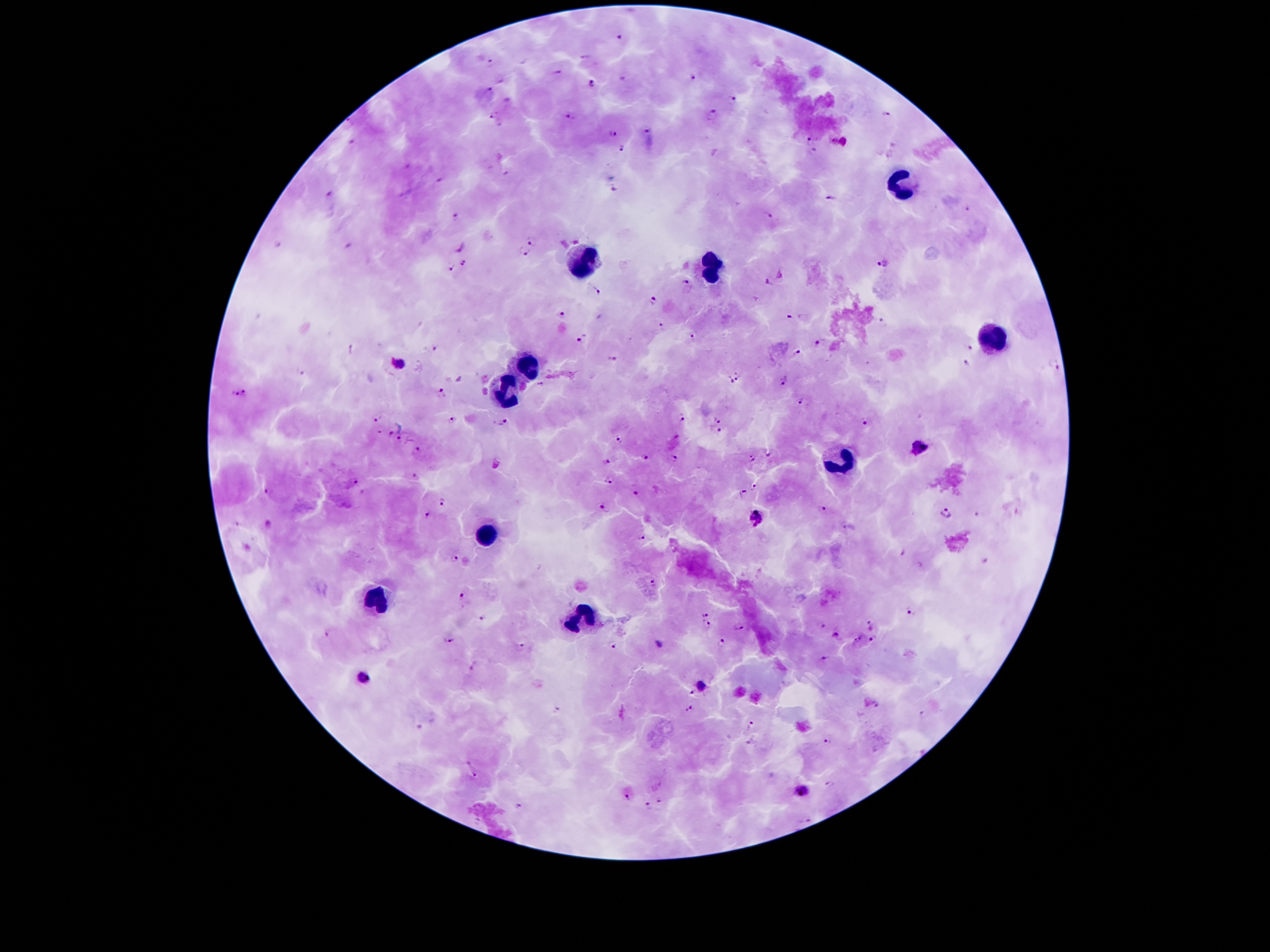
coordinate format = approximate object centers, in pixels from the top-left corner
Plasmodium parasite locations = (x=491, y=61), (x=558, y=72), (x=692, y=77), (x=591, y=84), (x=490, y=91), (x=733, y=100), (x=886, y=113), (x=493, y=115), (x=713, y=115), (x=570, y=116), (x=351, y=122), (x=647, y=131), (x=614, y=133), (x=813, y=139), (x=353, y=141), (x=833, y=141), (x=845, y=141), (x=623, y=147), (x=814, y=150), (x=508, y=173), (x=441, y=180), (x=614, y=190), (x=329, y=195), (x=831, y=199), (x=967, y=209), (x=767, y=216), (x=455, y=217), (x=533, y=241), (x=281, y=242), (x=459, y=247), (x=524, y=251), (x=463, y=264), (x=882, y=265), (x=450, y=268), (x=781, y=273), (x=686, y=283), (x=769, y=283), (x=597, y=292), (x=653, y=301), (x=561, y=315), (x=790, y=316), (x=882, y=320), (x=664, y=327), (x=693, y=338), (x=580, y=339), (x=819, y=341), (x=436, y=346), (x=969, y=348), (x=351, y=350), (x=798, y=352), (x=612, y=360), (x=398, y=362), (x=966, y=363), (x=1055, y=363), (x=735, y=371), (x=302, y=373), (x=461, y=378), (x=738, y=380), (x=729, y=381), (x=783, y=382), (x=541, y=384), (x=245, y=390), (x=442, y=392), (x=237, y=395), (x=800, y=401), (x=680, y=418), (x=378, y=419), (x=452, y=420), (x=718, y=421), (x=866, y=422), (x=503, y=423), (x=720, y=430), (x=378, y=432), (x=390, y=433), (x=399, y=438), (x=618, y=438), (x=921, y=446), (x=417, y=450), (x=769, y=456), (x=644, y=457), (x=675, y=458), (x=752, y=459), (x=605, y=460), (x=416, y=474), (x=609, y=478), (x=352, y=483), (x=752, y=486), (x=268, y=489), (x=744, y=491), (x=636, y=493), (x=442, y=500), (x=601, y=505), (x=822, y=508), (x=426, y=513), (x=946, y=514), (x=979, y=514), (x=756, y=518), (x=236, y=524), (x=845, y=526), (x=641, y=538), (x=901, y=552), (x=454, y=558), (x=983, y=560), (x=653, y=583), (x=462, y=596), (x=909, y=611), (x=704, y=615), (x=484, y=618), (x=870, y=623), (x=708, y=624), (x=822, y=625), (x=739, y=626), (x=325, y=632), (x=835, y=634), (x=449, y=639), (x=857, y=639), (x=871, y=640), (x=720, y=644), (x=613, y=645), (x=660, y=645), (x=523, y=647), (x=825, y=657), (x=364, y=678), (x=702, y=686), (x=878, y=705), (x=689, y=708), (x=558, y=710), (x=925, y=713), (x=752, y=724), (x=421, y=725), (x=827, y=741), (x=748, y=744), (x=474, y=776), (x=829, y=783), (x=803, y=791), (x=627, y=800), (x=661, y=801), (x=648, y=805), (x=520, y=807), (x=807, y=821)
leukocyte locations = (x=900, y=182), (x=586, y=257), (x=718, y=266), (x=991, y=338), (x=529, y=362), (x=507, y=391), (x=843, y=460), (x=486, y=533), (x=378, y=598), (x=580, y=617)
field of view = one from this slide
patient malaria status = infected with Plasmodium falciparum
preparation = thick peripheral-blood smear
magnification = 100x
stain = Giemsa
image size = 1270×952 pixels
capture = smartphone camera through the microscope eyepiece